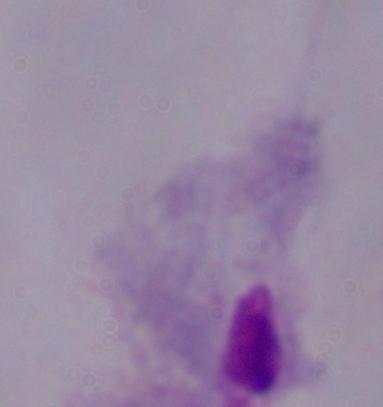

Photomicrograph. 1000x magnification. A trichomonad is shown.